Comment on the morphology of the erythrocytes.
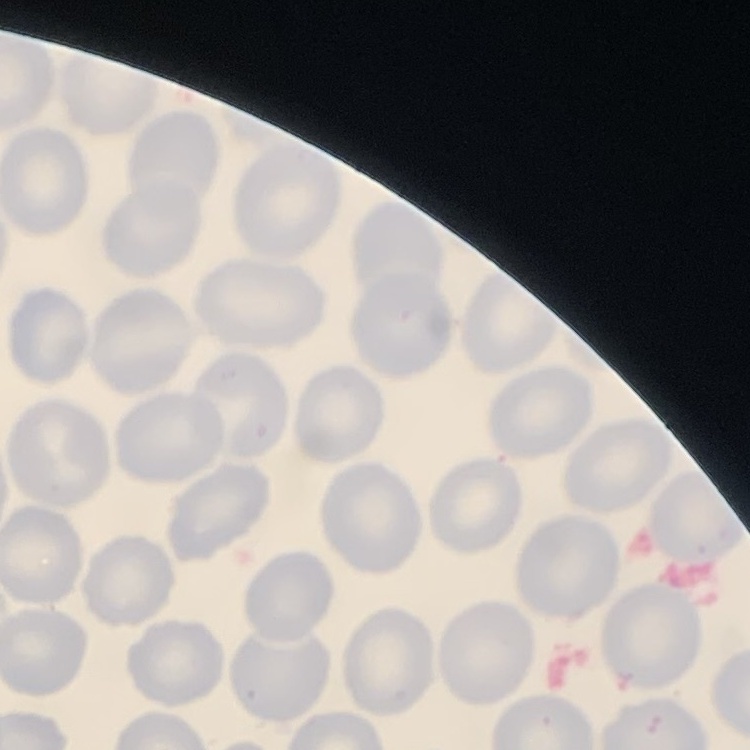

They show no rouleaux formation.

{
  "stain": "Field's or Giemsa",
  "preparation": "thin blood film",
  "image_type": "one tile cut from a larger photomicrograph"
}